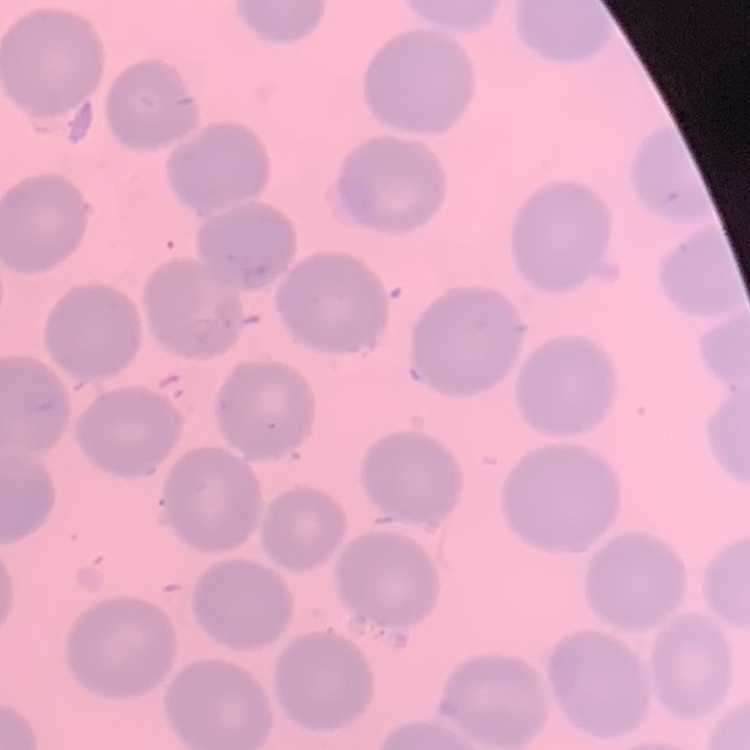

The erythrocytes show no rouleaux formation. Field's or Giemsa stain. Square crop of a larger photomicrograph. Thin blood smear.